Locate every blood parasite and identify its species.
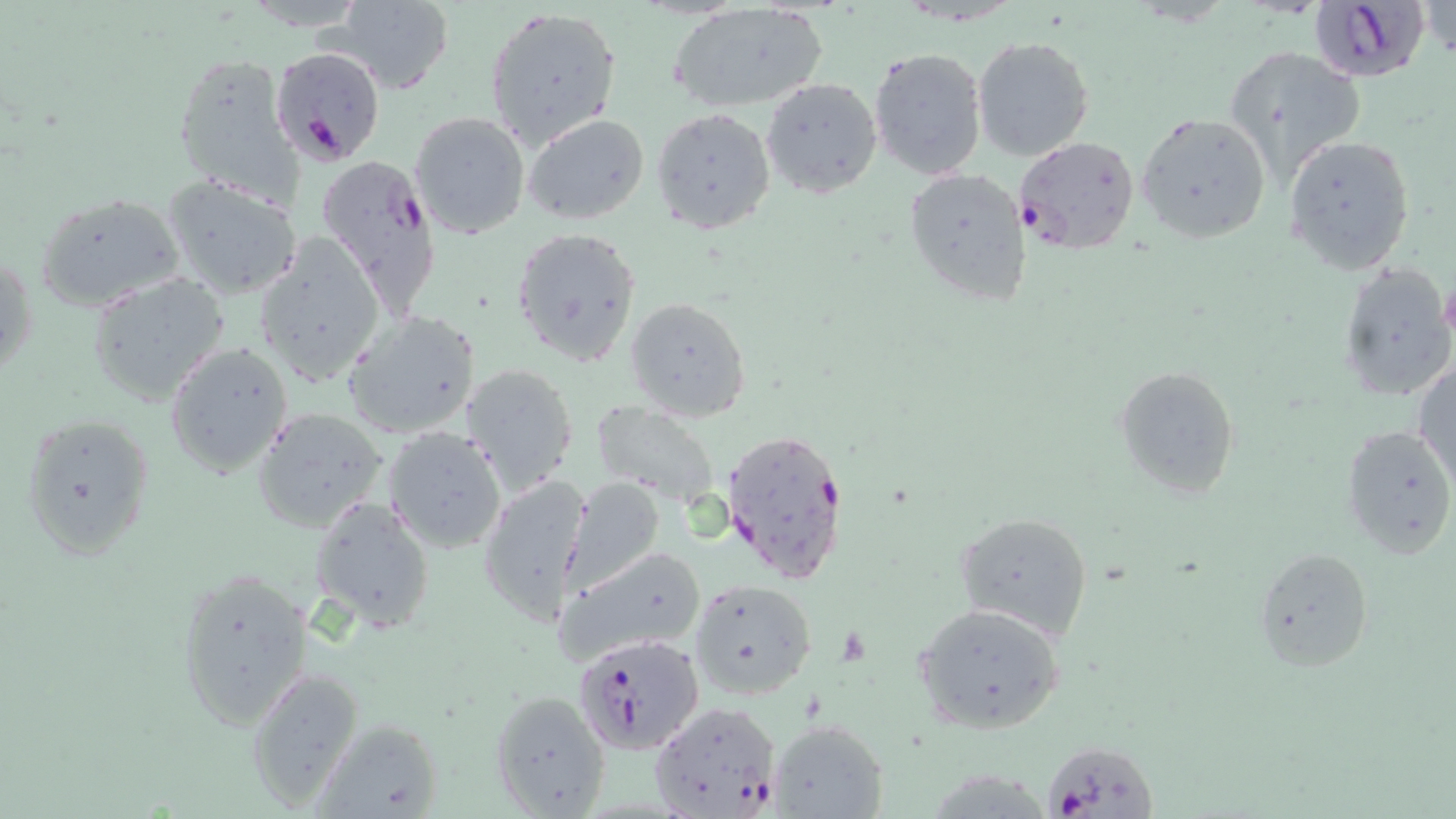

Approximate bounding boxes as [x1, y1, x2, y2] in pixels.
Plasmodium falciparum-infected red blood cells: [1306, 1, 1432, 83], [269, 48, 387, 169], [1013, 136, 1140, 254], [314, 155, 439, 301], [721, 427, 851, 589], [575, 633, 706, 752], [647, 699, 784, 817], [1043, 740, 1157, 819].
No Plasmodium ovale, Plasmodium malariae, Plasmodium vivax, Babesia divergens, or Trypanosoma brucei observed.

Summary:
  - Uninfected red blood cell locations: [327, 0, 454, 93], [1419, 2, 1455, 59], [669, 3, 828, 114], [483, 7, 622, 150], [971, 34, 1095, 161], [868, 45, 990, 181], [1224, 47, 1366, 187], [171, 51, 299, 206], [761, 77, 882, 199], [652, 108, 775, 234], [408, 111, 531, 241], [522, 112, 650, 225], [1136, 112, 1272, 244], [1285, 134, 1416, 273], [903, 166, 1032, 306], [160, 173, 303, 300], [37, 192, 187, 313], [510, 227, 642, 366], [251, 235, 386, 386], [2, 251, 36, 385], [1337, 262, 1454, 403], [87, 273, 229, 406], [625, 297, 751, 422], [344, 309, 482, 439], [165, 340, 294, 477], [1414, 361, 1456, 487], [461, 363, 579, 495], [1114, 367, 1240, 497], [592, 403, 719, 507], [251, 407, 389, 533], [20, 412, 155, 562], [1342, 423, 1456, 557], [384, 426, 507, 554], [480, 475, 593, 625], [564, 476, 665, 589], [309, 497, 435, 633], [956, 511, 1094, 640], [556, 544, 707, 663], [1253, 546, 1375, 671], [176, 565, 314, 732], [688, 577, 816, 699], [915, 604, 1067, 734], [246, 670, 362, 809], [489, 688, 612, 815], [311, 717, 445, 819], [770, 720, 889, 817]
  - Platelet locations: [1439, 282, 1456, 338]
  - Slide-level diagnosis: Plasmodium falciparum
  - Field of view: single
  - Modality: optical microscopy
  - Preparation: thin blood smear
  - Image size: 1456×819 pixels
  - Stain: May-Grünwald-Giemsa
  - Magnification: 1000x